Report the malaria status of this cell.
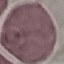
It is uninfected.

Summary:
  - Capture: smartphone camera at the microscope eyepiece
  - Image type: cell patch, automatically extracted from a larger field of view and resized to 64 × 64 pixels
  - Stain: Giemsa
  - Preparation: thin blood smear